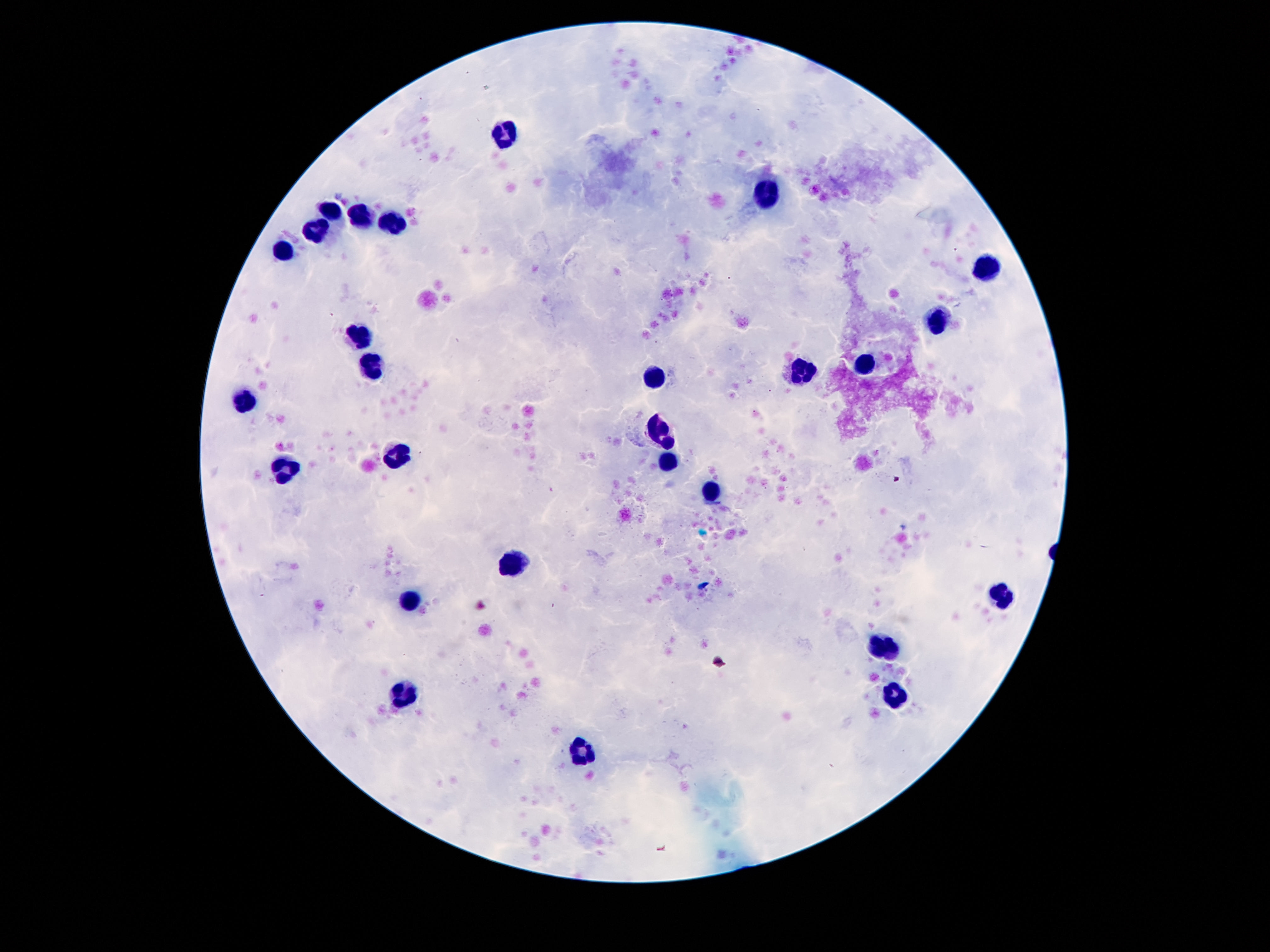
{
  "stain": "Giemsa",
  "image_size": "1270×952 pixels",
  "field_of_view": "single",
  "leukocyte_locations": "approximate centers as (x, y) in pixels: (503, 133), (766, 193), (331, 209), (361, 215), (394, 220), (318, 226), (279, 250), (986, 267), (936, 321), (359, 336), (372, 363), (868, 365), (801, 373), (654, 379), (245, 402), (661, 428), (394, 454), (665, 459), (284, 469), (712, 493), (512, 563), (1001, 596), (409, 602), (883, 645), (896, 697), (402, 698), (583, 754)",
  "patient_malaria_status": "uninfected",
  "capture": "smartphone camera through the microscope eyepiece",
  "preparation": "thick peripheral-blood smear",
  "magnification": "100x"
}